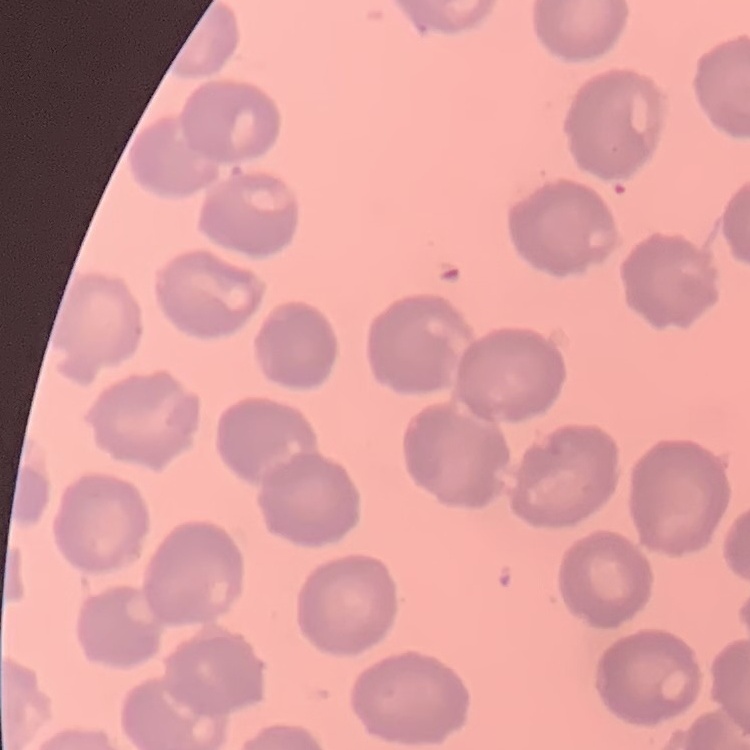
The erythrocytes exhibit no rouleaux formation. Square crop of a larger photomicrograph. Thin blood film. Field's or Giemsa stain.